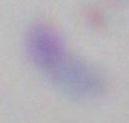

Summary:
  - Identification: Toxoplasma gondii
  - Magnification: 1000x
  - Modality: micrograph